Assess this cell for malaria.
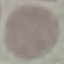

It is uninfected.

Automatically extracted cell patch, resized to 64 × 64 pixels. Acquired by smartphone through the microscope eyepiece. Thin smear of blood. Giemsa stain.